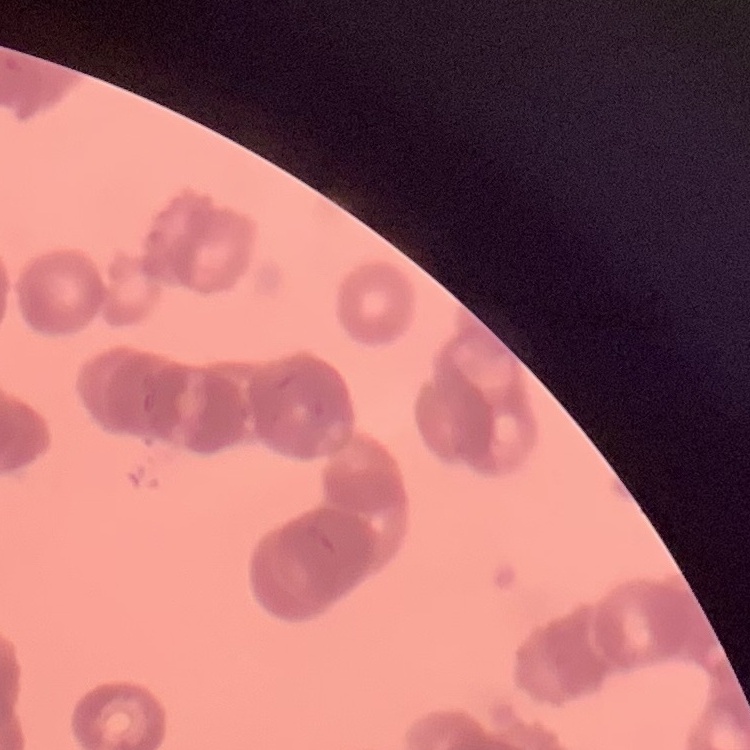
red_blood_cell_morphology: rouleaux formation
stain: Field's or Giemsa
image_type: square crop of a larger photomicrograph
preparation: thin blood film